Assess this cell for malaria.
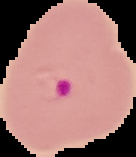

It is parasitized.

Summary:
  - Image type: segmented cell region with the area outside set to black
  - Image size: 136×157 pixels
  - Preparation: thin blood film